Outline each Plasmodium vivax-infected red blood cell.
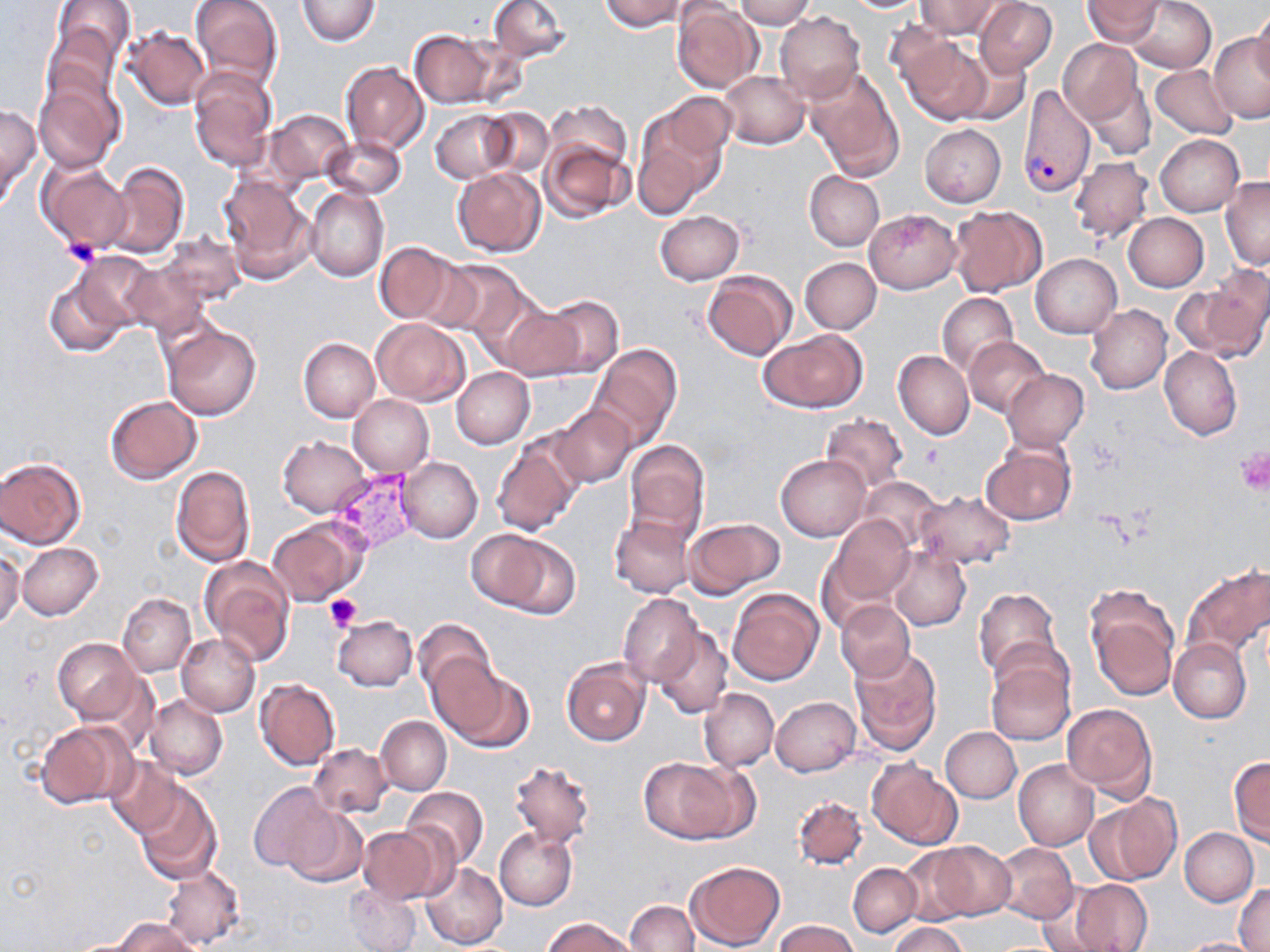
Approximate bounding boxes as [x1, y1, x2, y2] in pixels.
Plasmodium vivax-infected red blood cells: [1019, 84, 1095, 197], [328, 470, 420, 554].

Summary:
  - Uninfected red blood cell locations: [189, 0, 283, 90], [296, 0, 381, 45], [488, 0, 569, 61], [599, 0, 687, 31], [735, 0, 815, 28], [1084, 0, 1163, 44], [1125, 0, 1216, 72], [50, 1, 133, 69], [845, 1, 925, 12], [915, 1, 1001, 38], [976, 1, 1057, 75], [673, 3, 763, 92], [1251, 5, 1270, 89], [775, 12, 865, 104], [44, 19, 123, 108], [887, 23, 969, 106], [123, 27, 211, 111], [409, 29, 503, 109], [1209, 33, 1269, 123], [904, 37, 992, 125], [1057, 39, 1142, 123], [952, 51, 1030, 127], [340, 61, 429, 155], [1150, 64, 1238, 139], [188, 68, 277, 172], [804, 68, 904, 177], [722, 70, 808, 148], [34, 77, 123, 173], [1084, 82, 1155, 160], [663, 92, 737, 156], [547, 100, 630, 171], [0, 103, 39, 201], [481, 107, 553, 178], [265, 109, 351, 185], [432, 110, 514, 182], [634, 121, 714, 216], [920, 123, 1006, 207], [1155, 134, 1245, 217], [322, 136, 406, 200], [541, 138, 631, 223], [1070, 156, 1154, 244], [105, 162, 189, 257], [38, 163, 130, 254], [452, 168, 545, 256], [805, 171, 884, 250], [220, 175, 314, 283], [1221, 177, 1270, 269], [306, 187, 388, 282], [949, 206, 1046, 296], [864, 209, 961, 293], [656, 211, 744, 285], [1122, 212, 1208, 292], [159, 232, 245, 306], [373, 241, 459, 324], [75, 254, 159, 336], [1031, 254, 1121, 339], [800, 258, 881, 334], [441, 259, 532, 344], [121, 260, 212, 340], [42, 269, 135, 359], [703, 271, 796, 360], [1178, 276, 1270, 361], [937, 293, 1018, 376], [534, 295, 624, 380], [1087, 304, 1172, 394], [502, 308, 586, 381], [372, 319, 469, 405], [161, 322, 262, 421], [759, 329, 867, 413], [298, 337, 380, 422], [964, 337, 1050, 416], [589, 345, 683, 449], [1159, 346, 1242, 441], [893, 350, 974, 439], [453, 368, 535, 449], [1003, 371, 1088, 451], [349, 394, 434, 477], [105, 396, 202, 484], [550, 404, 637, 488], [820, 414, 908, 491], [491, 435, 584, 537], [278, 436, 371, 517], [624, 439, 710, 538], [980, 440, 1075, 526], [775, 455, 870, 541], [397, 457, 483, 544], [0, 458, 86, 548], [170, 464, 255, 566], [858, 475, 940, 549], [913, 490, 1015, 568], [609, 514, 696, 599], [828, 514, 915, 605], [684, 517, 783, 598], [268, 519, 367, 605], [464, 529, 552, 606], [492, 532, 580, 618], [17, 543, 103, 621], [888, 546, 971, 631], [0, 549, 24, 631], [200, 558, 296, 666], [1182, 565, 1270, 657], [1084, 583, 1180, 699], [973, 587, 1062, 683], [728, 588, 823, 685], [117, 593, 194, 677], [617, 593, 703, 685], [836, 600, 915, 681], [331, 615, 418, 691], [412, 617, 496, 702], [652, 626, 734, 720], [177, 633, 260, 717], [1168, 637, 1252, 723], [52, 639, 140, 721], [848, 647, 943, 756], [985, 652, 1075, 746], [436, 658, 532, 752], [561, 658, 650, 746], [254, 679, 340, 771], [698, 688, 778, 772], [145, 694, 227, 779], [771, 696, 861, 775], [1060, 702, 1156, 801], [377, 716, 451, 795], [34, 720, 136, 808], [941, 727, 1020, 803], [309, 744, 392, 818], [105, 756, 184, 839], [639, 756, 746, 843], [1228, 756, 1270, 844], [509, 759, 596, 847], [868, 759, 963, 851], [1013, 759, 1099, 850], [134, 781, 220, 882], [248, 782, 339, 874], [402, 786, 489, 870], [1088, 793, 1182, 886], [793, 795, 868, 868], [283, 807, 368, 888], [356, 825, 451, 904], [493, 828, 578, 910], [1180, 828, 1258, 905], [922, 841, 1016, 922], [992, 843, 1078, 924], [898, 845, 978, 925], [686, 860, 786, 951], [420, 861, 508, 951], [848, 863, 921, 936], [160, 864, 245, 949], [1069, 879, 1153, 952], [345, 883, 421, 952], [1235, 885, 1270, 951], [625, 901, 698, 952], [544, 917, 636, 952], [110, 918, 198, 952], [774, 920, 861, 952], [888, 922, 967, 952], [1178, 937, 1262, 951]
  - Platelet locations: [61, 237, 102, 268], [919, 445, 943, 468], [1233, 446, 1270, 495], [326, 594, 362, 631]
  - Slide-level diagnosis: Plasmodium vivax
  - Field of view: single
  - Image size: 1270×952 pixels
  - Magnification: 1000x
  - Preparation: thin blood smear
  - Modality: light microscopy
  - Stain: May-Grünwald-Giemsa